State which cell type is depicted.
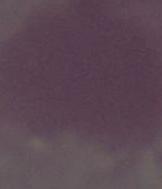
An erythrocyte.

modality: photomicrograph
magnification: 1000x